Report the malaria status of this cell.
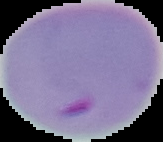
Parasitized.

From a thin blood film. Image is 163×142 pixels. Cell region segmented out of the field of view; the surrounding area is masked to black.